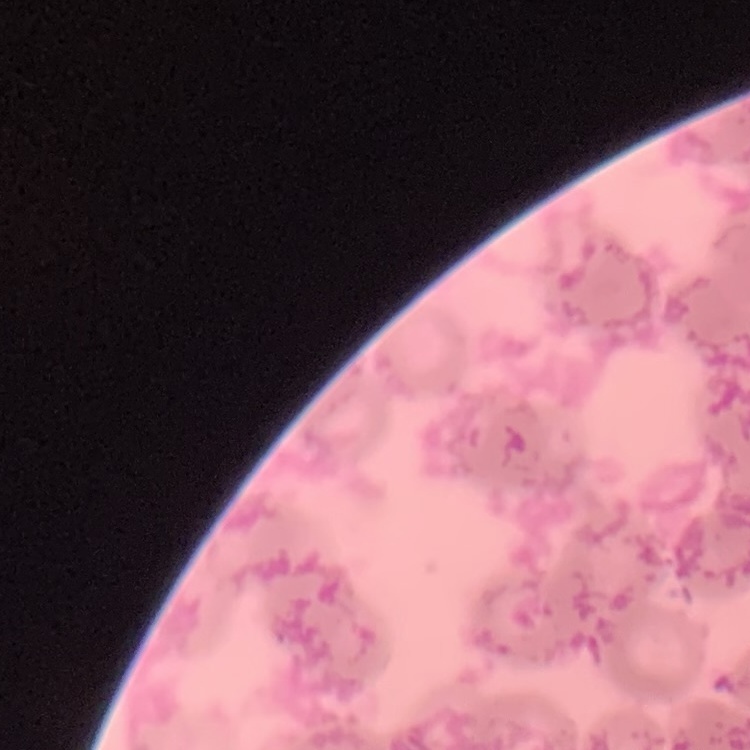
erythrocyte morphology = rouleaux formation
stain = Field's or Giemsa
image type = one tile cut from a larger photomicrograph
preparation = thin blood film